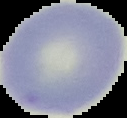

Summary:
  - Image type: segmented cell region with the area outside set to black
  - Image size: 127×118 pixels
  - Result: no malaria parasites seen
  - Preparation: thin blood film